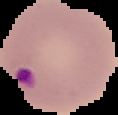
preparation = thin blood film
image type = segmented cell region on a black background
result = Plasmodium parasites identified
image size = 118×115 pixels